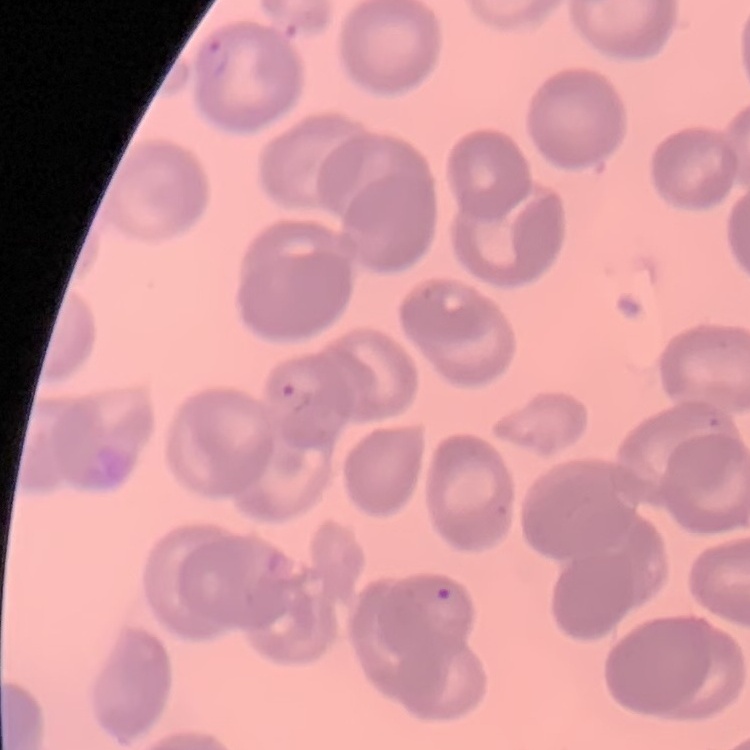
red_blood_cell_morphology: no rouleaux formation
image_type: one tile cut from a larger photomicrograph
preparation: thin blood smear
stain: Field's or Giemsa